Give the extent of all Plasmodium malariae-infected red blood cells.
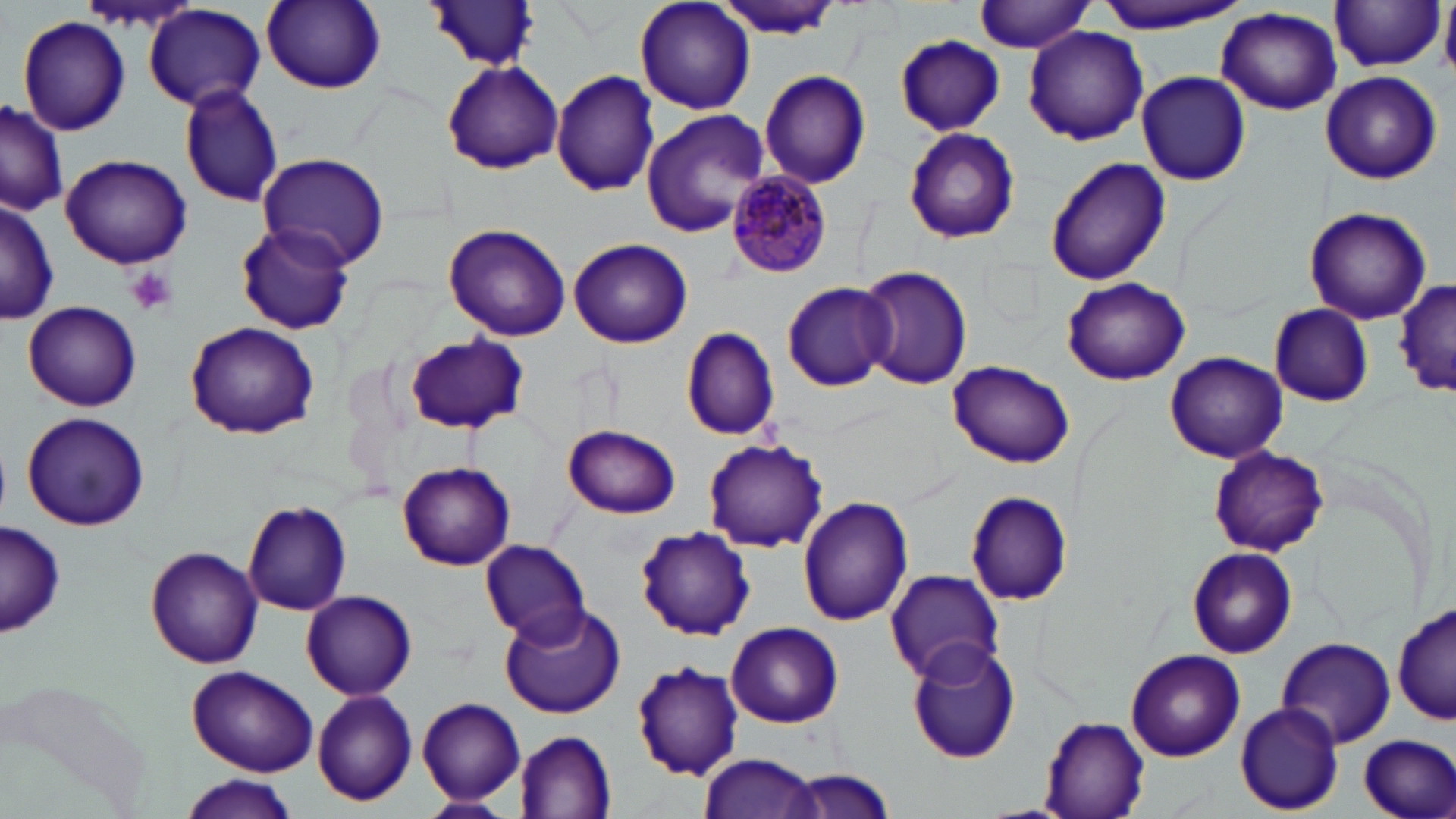

Approximate bounding boxes as (x1, y1, x2, y2) in pixels.
Plasmodium malariae-infected red blood cells: (725, 172, 832, 277).

Summary:
  - Platelet locations: (127, 267, 177, 318)
  - Uninfected red blood cell locations: (259, 0, 388, 95), (633, 0, 757, 116), (714, 0, 844, 40), (1091, 0, 1250, 32), (1440, 1, 1456, 77), (424, 2, 545, 74), (974, 2, 1098, 53), (1329, 2, 1446, 73), (144, 4, 266, 111), (1215, 7, 1343, 115), (16, 15, 132, 136), (1024, 25, 1148, 146), (895, 34, 1006, 135), (442, 61, 562, 174), (759, 68, 871, 189), (551, 69, 661, 196), (1136, 69, 1251, 186), (1320, 69, 1442, 183), (176, 83, 286, 208), (0, 100, 67, 220), (641, 109, 770, 239), (903, 126, 1021, 245), (258, 152, 391, 269), (61, 154, 192, 270), (1044, 157, 1171, 286), (0, 197, 59, 325), (1304, 207, 1432, 323), (237, 221, 357, 335), (444, 223, 573, 341), (568, 238, 692, 349), (858, 265, 974, 390), (1061, 276, 1190, 385), (1396, 279, 1456, 398), (781, 280, 894, 389), (22, 300, 143, 412), (1267, 304, 1374, 406), (182, 320, 320, 440), (680, 326, 780, 441), (404, 333, 529, 436), (1165, 352, 1288, 464), (948, 358, 1075, 469), (20, 411, 150, 533), (563, 424, 681, 519), (702, 437, 828, 553), (1210, 447, 1328, 556), (397, 462, 516, 571), (965, 489, 1073, 605), (799, 495, 914, 627), (242, 499, 352, 615), (1, 520, 65, 639), (635, 525, 757, 640), (479, 539, 590, 644), (1185, 545, 1299, 658), (146, 546, 263, 668), (883, 569, 1005, 685), (301, 589, 417, 700), (499, 603, 626, 719), (1392, 604, 1456, 725), (726, 621, 846, 728), (1277, 634, 1396, 746), (907, 639, 1022, 763), (1125, 647, 1246, 762), (631, 660, 743, 780), (187, 666, 319, 777), (0, 671, 156, 819), (311, 687, 420, 806), (418, 697, 525, 804), (1235, 704, 1345, 814), (1039, 716, 1151, 818), (516, 731, 616, 816), (1356, 735, 1455, 819), (698, 753, 823, 819), (772, 770, 904, 818), (174, 777, 301, 818), (418, 795, 513, 817)
  - Slide-level diagnosis: Plasmodium malariae
  - Magnification: 1000x
  - Field of view: single
  - Image size: 1456×819 pixels
  - Modality: light microscopy
  - Stain: May-Grünwald-Giemsa
  - Preparation: thin blood smear